State the preparation type.
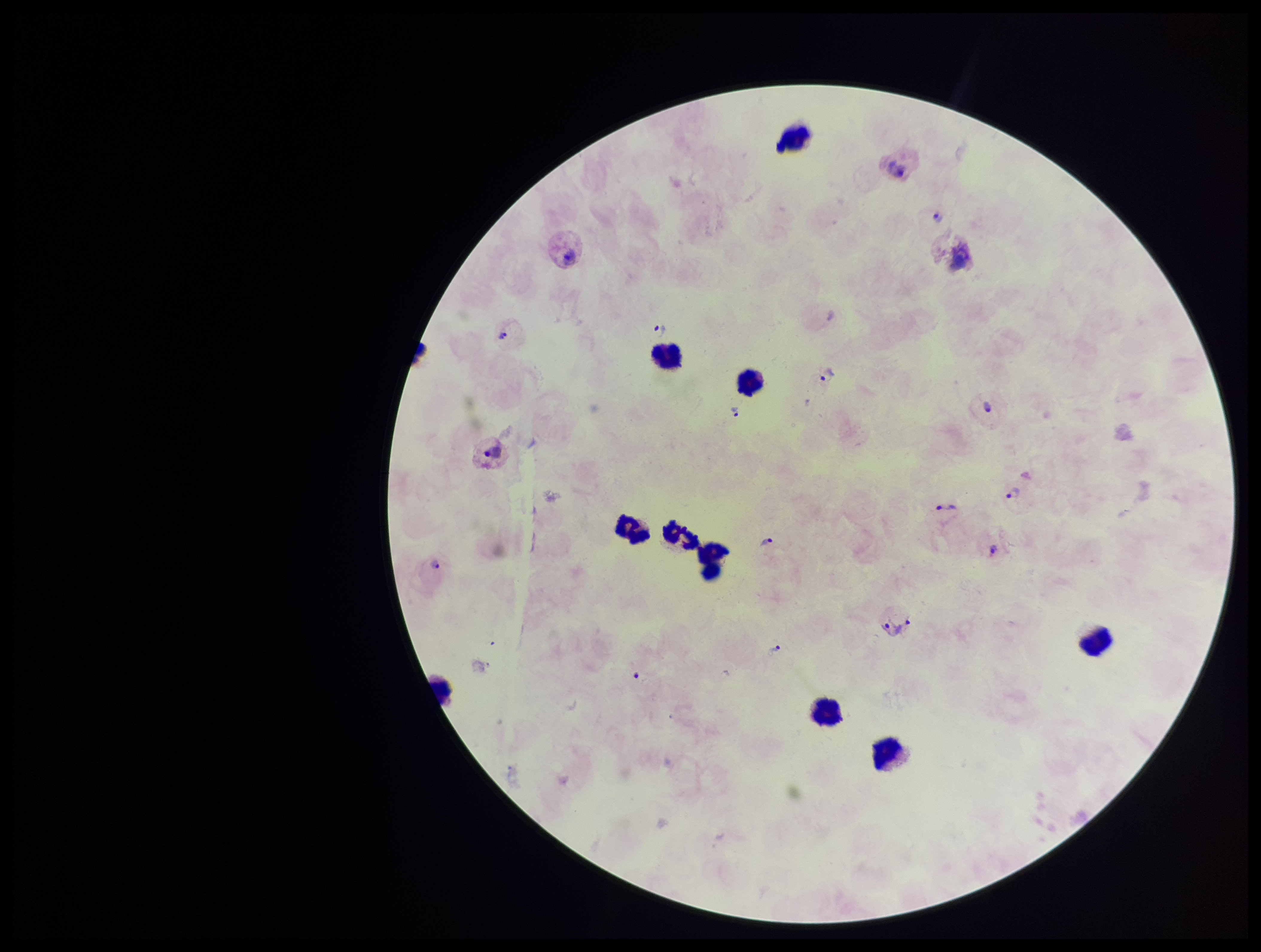

A thick smear.

Summary:
  - Capture: smartphone photograph through the microscope eyepiece
  - Patient malaria status: positive
  - Image size: 1261×952 pixels
  - Species reported for this patient: Plasmodium vivax
  - Parasite count: 18
  - Field of view: single
  - Leukocyte count: 10
  - Stain: Giemsa
  - Plasmodium parasites: seen